Locate and identify every blood parasite.
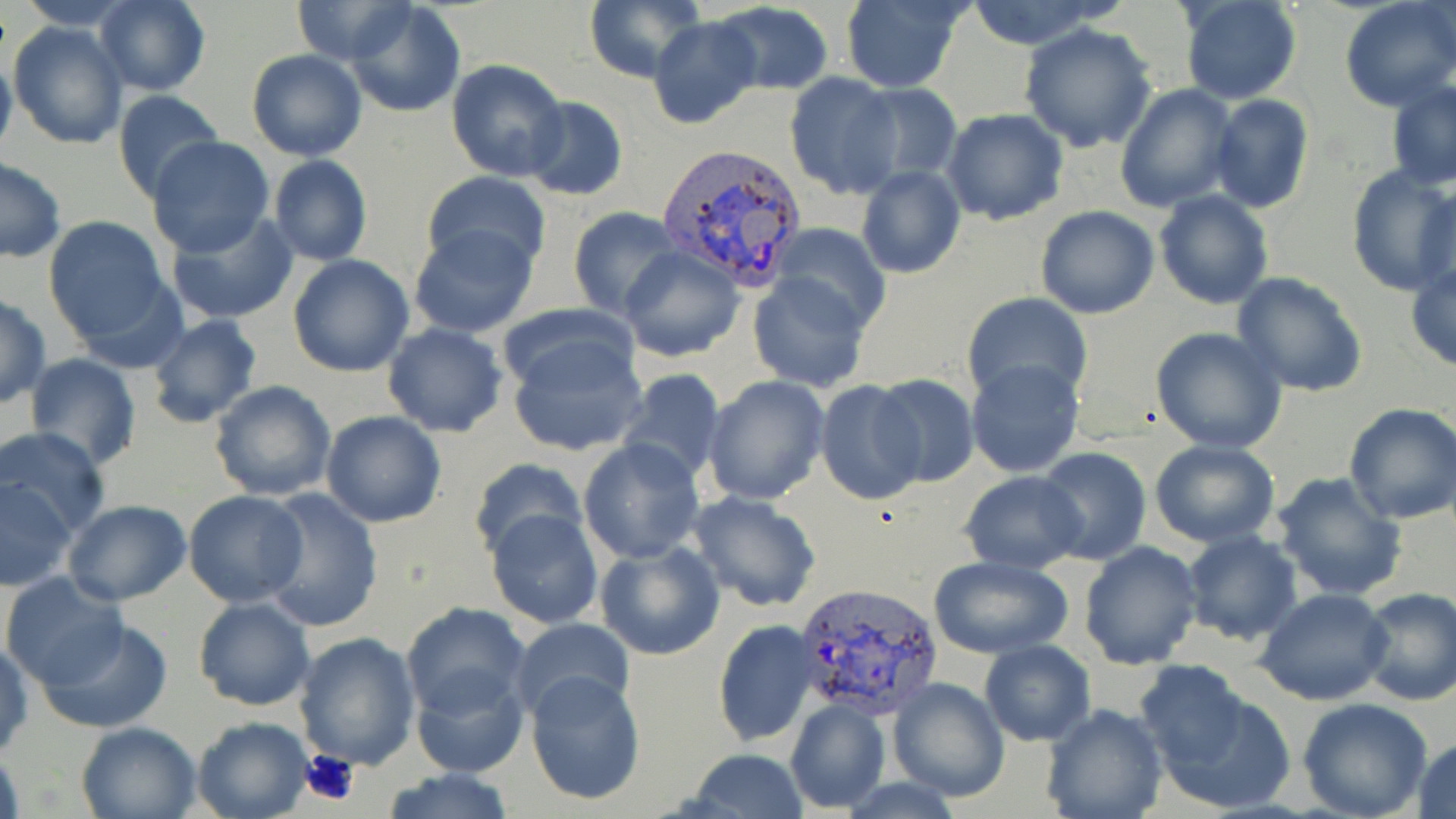
Approximate bounding boxes as [x1, y1, x2, y2] in pixels.
Plasmodium vivax-infected red blood cells: [655, 142, 808, 290], [794, 580, 945, 719].
No Plasmodium falciparum, Plasmodium ovale, Plasmodium malariae, Babesia divergens, or Trypanosoma brucei observed.

Summary:
  - Uninfected red blood cell locations: [10, 0, 144, 31], [95, 0, 211, 97], [290, 0, 416, 65], [962, 0, 1110, 50], [1178, 0, 1302, 105], [345, 1, 466, 118], [584, 1, 702, 83], [839, 1, 969, 94], [1339, 2, 1456, 112], [712, 3, 835, 94], [648, 16, 762, 130], [8, 19, 129, 151], [1020, 22, 1159, 154], [246, 49, 367, 161], [0, 50, 17, 164], [445, 59, 569, 183], [785, 72, 902, 197], [1386, 76, 1456, 192], [850, 83, 962, 186], [1114, 84, 1238, 211], [112, 90, 228, 204], [1208, 93, 1315, 215], [521, 95, 629, 202], [942, 109, 1070, 226], [146, 136, 277, 258], [268, 155, 373, 266], [1, 158, 67, 264], [1346, 164, 1453, 295], [856, 166, 967, 279], [421, 171, 549, 275], [1409, 179, 1455, 298], [1153, 190, 1274, 310], [1034, 204, 1161, 320], [567, 207, 685, 318], [167, 212, 298, 326], [42, 216, 175, 348], [768, 221, 891, 331], [408, 224, 540, 338], [618, 245, 746, 363], [1406, 253, 1456, 375], [287, 254, 414, 378], [1231, 271, 1368, 397], [746, 272, 875, 393], [962, 292, 1093, 409], [0, 294, 50, 408], [495, 303, 637, 394], [144, 314, 262, 429], [382, 323, 510, 438], [1150, 326, 1288, 455], [502, 333, 649, 457], [24, 354, 143, 472], [966, 359, 1085, 478], [616, 368, 727, 484], [702, 373, 831, 504], [870, 377, 980, 487], [209, 379, 338, 501], [815, 380, 925, 506], [1343, 401, 1456, 525], [322, 411, 448, 528], [1, 427, 110, 538], [576, 439, 707, 565], [1149, 439, 1280, 548], [1037, 448, 1151, 565], [0, 449, 131, 597], [468, 457, 588, 565], [958, 469, 1089, 573], [1271, 471, 1407, 601], [1, 477, 77, 590], [257, 489, 384, 634], [686, 489, 822, 612], [184, 491, 309, 608], [63, 499, 192, 606], [484, 509, 603, 630], [1182, 529, 1304, 645], [1079, 540, 1203, 668], [595, 541, 726, 661], [929, 554, 1073, 658], [3, 573, 128, 690], [1355, 586, 1455, 706], [1257, 588, 1393, 705], [192, 598, 315, 712], [400, 600, 531, 718], [508, 616, 636, 721], [36, 618, 176, 734], [711, 618, 822, 748], [294, 633, 422, 771], [1, 637, 32, 765], [979, 640, 1096, 746], [411, 665, 527, 777], [524, 669, 647, 805], [1142, 672, 1293, 814], [889, 676, 1011, 802], [1297, 697, 1433, 818], [784, 698, 890, 813], [1041, 704, 1167, 819], [191, 716, 313, 819], [75, 720, 202, 818], [1412, 737, 1456, 819], [687, 749, 808, 819], [376, 768, 517, 819]
  - Slide-level diagnosis: Plasmodium vivax
  - Modality: light microscopy
  - Stain: May-Grünwald-Giemsa
  - Preparation: thin blood film
  - Field of view: one of a larger specimen
  - Image size: 1456×819 pixels
  - Magnification: 1000x